Locate every Plasmodium parasite.
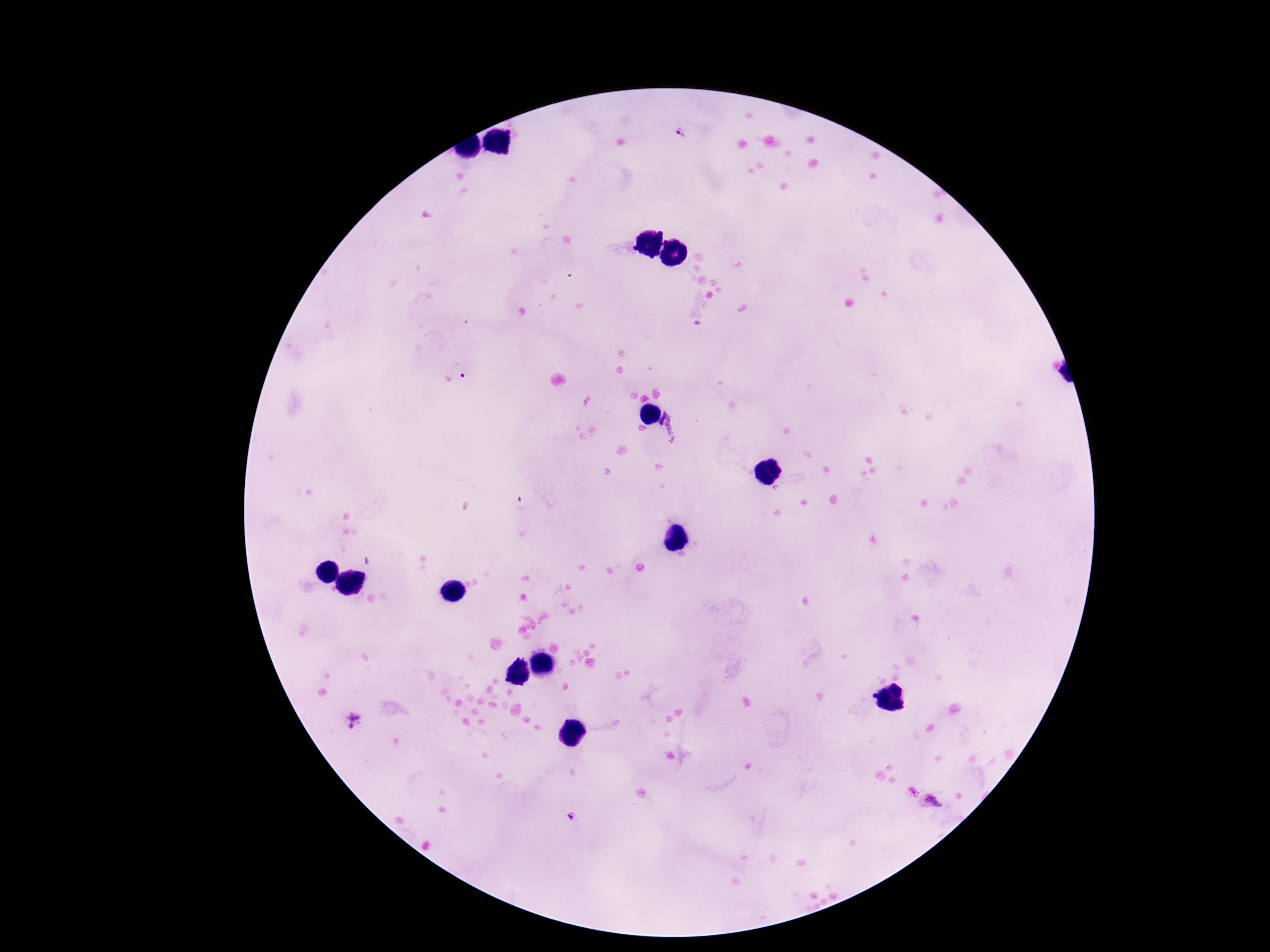
Approximate object centers, in pixels from the top-left corner.
Plasmodium parasites: (x=680, y=132), (x=456, y=372), (x=675, y=424), (x=354, y=721), (x=932, y=804), (x=573, y=816).

Image is 1270×952 pixels. 100x magnification. Thick peripheral-blood smear. Single field of view. Smartphone photograph taken through the microscope eyepiece. Giemsa-stained preparation. Patient malaria status: infected.